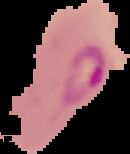 Cell region segmented out of the field of view; the surrounding area is masked to black. Result: Plasmodium parasites detected. From a thin blood film. Image is 130×154 pixels.